Report the malaria status of this cell.
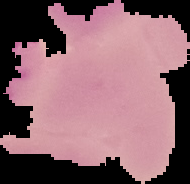
Uninfected.

image type = segmented cell region on a black background
image size = 190×184 pixels
preparation = thin blood film